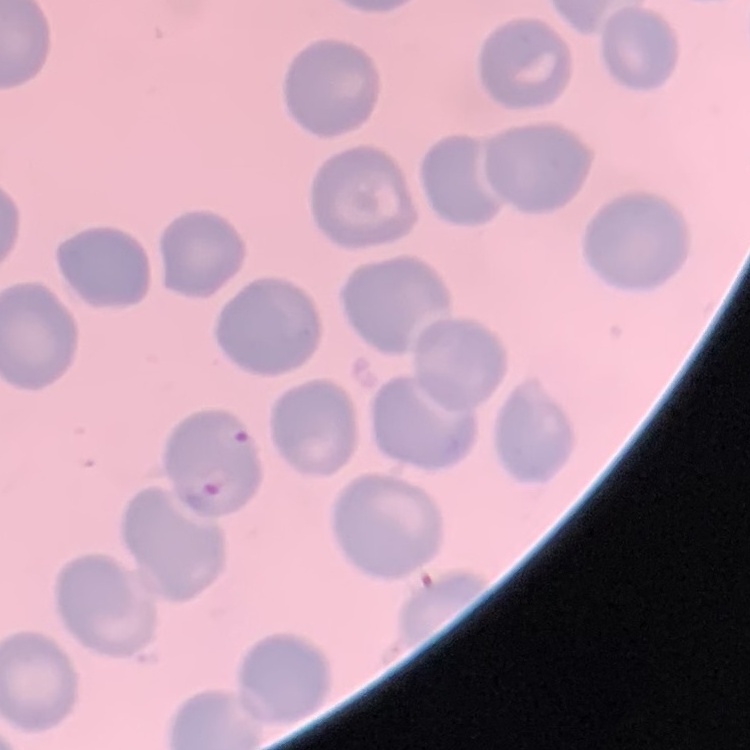
{
  "erythrocyte_morphology": "no rouleaux formation",
  "stain": "Field's or Giemsa",
  "image_type": "square crop of a larger photomicrograph",
  "preparation": "thin blood smear"
}